Assess this cell for malaria.
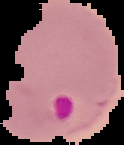

It is parasitized.

Image is 124×145 pixels. From a thin blood film. The area outside the segmented cell region is set to black.